Give the position of every malaria parasite.
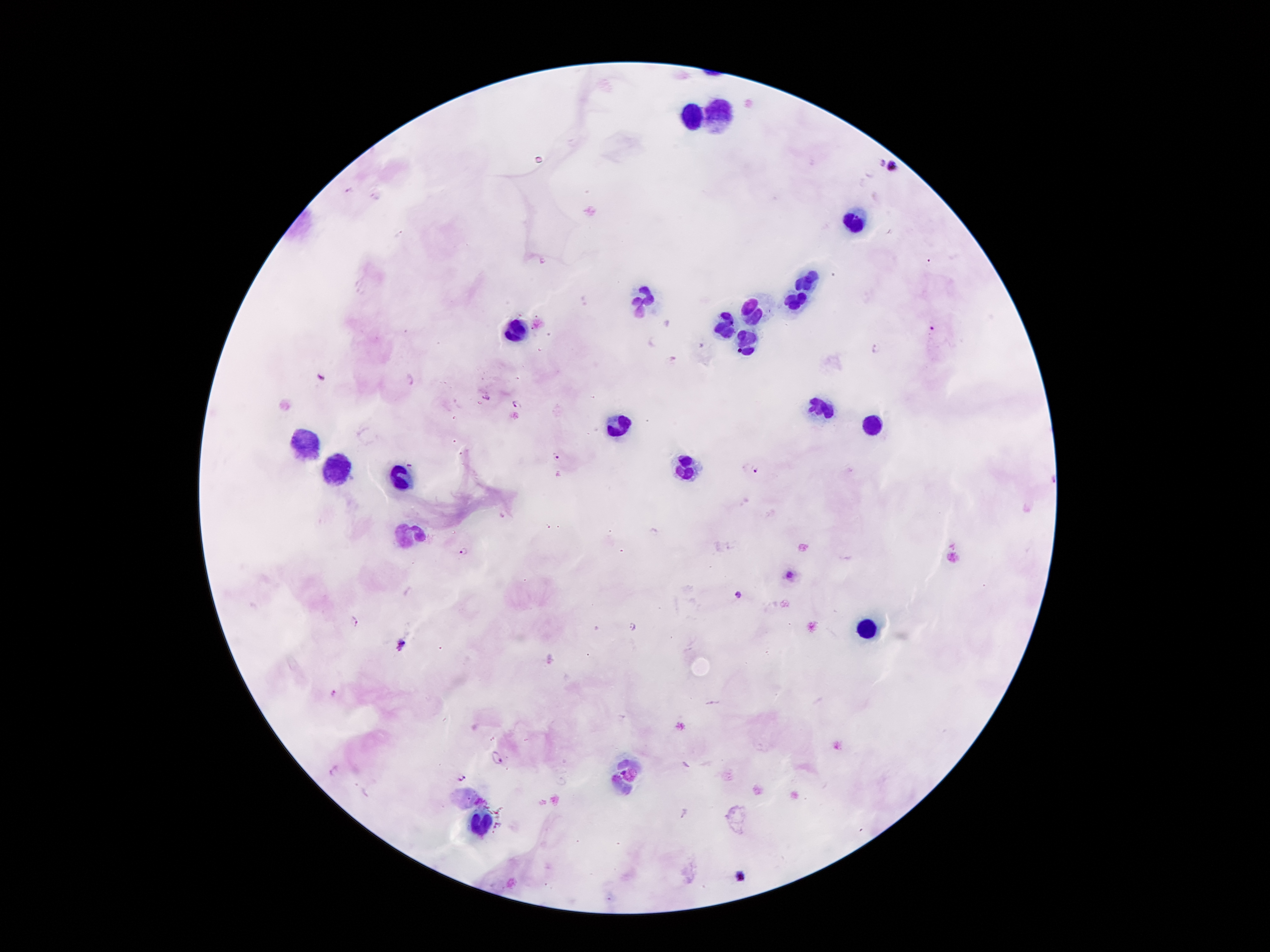

Approximate centers as [x, y] in pixels.
Malaria parasites: [878, 163], [895, 167], [349, 191], [375, 197], [401, 235], [543, 261], [932, 330], [875, 347], [672, 357], [320, 375], [409, 378], [486, 396], [518, 405], [556, 457], [409, 465], [757, 471], [503, 515], [464, 551], [791, 575], [739, 596], [354, 621], [632, 625], [401, 644], [333, 694], [496, 757], [333, 772], [623, 772], [462, 776], [741, 875].

leukocyte locations = [689, 115], [714, 117], [851, 224], [808, 279], [642, 297], [791, 301], [755, 311], [732, 322], [515, 331], [746, 342], [821, 411], [875, 424], [615, 426], [310, 440], [687, 465], [337, 470], [401, 479], [408, 533], [866, 631], [637, 770], [621, 785], [478, 820]
stain = Giemsa
magnification = 100x
image size = 1270×952 pixels
patient malaria status = infected with Plasmodium falciparum
preparation = thick blood film
capture = smartphone through the microscope eyepiece
field of view = one from this slide